Identify the blood parasite species.
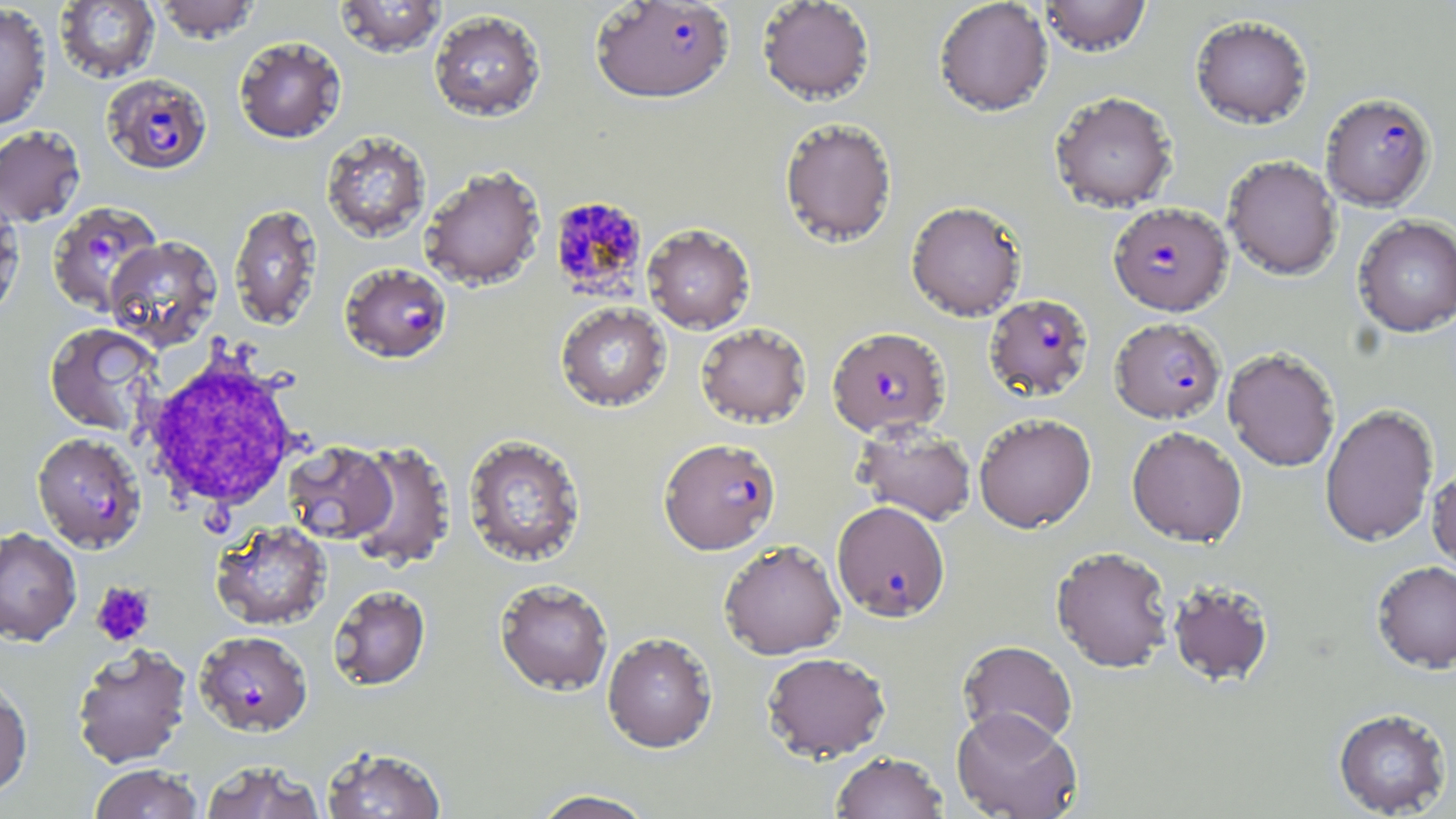

Plasmodium falciparum.

Approximate bounding boxes as (x1,y1)-(x2,y2) corner pairs in pixels. Uninfected red blood cell locations: (54,0)-(160,83), (154,0)-(260,43), (334,0)-(446,57), (757,0)-(876,105), (933,0)-(1053,117), (1038,0)-(1152,58), (0,3)-(51,130), (429,9)-(546,122), (1190,16)-(1313,130), (233,36)-(347,144), (1049,92)-(1178,213), (779,117)-(897,247), (0,125)-(86,226), (320,130)-(431,244), (1223,156)-(1342,280), (420,166)-(546,291), (0,194)-(25,321), (906,201)-(1027,321), (229,204)-(323,332), (1352,215)-(1456,338), (642,223)-(756,334), (104,236)-(222,351), (555,302)-(671,412), (44,322)-(161,436), (695,323)-(812,428), (1222,348)-(1341,472), (1320,403)-(1439,548), (973,413)-(1097,533), (852,422)-(976,525), (1126,426)-(1247,547), (462,434)-(587,568), (347,441)-(456,572), (284,442)-(396,544), (1427,462)-(1456,576), (211,520)-(331,631), (0,527)-(82,646), (718,540)-(846,660), (1051,546)-(1175,673), (1371,561)-(1456,674), (495,578)-(613,696), (1168,581)-(1275,688), (328,585)-(431,691), (602,632)-(717,753), (958,640)-(1077,748), (72,643)-(192,768), (762,651)-(891,762), (0,678)-(33,800), (951,707)-(1082,819), (1333,708)-(1451,817), (321,745)-(447,818), (830,751)-(948,819), (199,761)-(326,818), (88,764)-(204,819), (530,789)-(658,819). Plasmodium falciparum-infected red blood cell locations: (590,1)-(734,104), (102,73)-(212,176), (1321,93)-(1437,211), (548,196)-(648,300), (48,201)-(163,315), (1108,202)-(1232,316), (340,263)-(452,364), (983,294)-(1094,401), (1113,320)-(1229,426), (827,326)-(950,437), (32,433)-(149,553), (659,438)-(781,554), (832,501)-(950,622), (194,630)-(312,737). Platelet locations: (90,581)-(156,647). White blood cell locations: (136,348)-(307,517). Thin blood smear. Light microscopy. Captured at 1000x magnification. Image is 1456×819 pixels. One field of a larger specimen. May-Grünwald-Giemsa-stained preparation.